Identify the parasite.
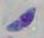

This is Toxoplasma gondii.

modality: micrograph
magnification: 1000x